Assess the morphology of the erythrocytes.
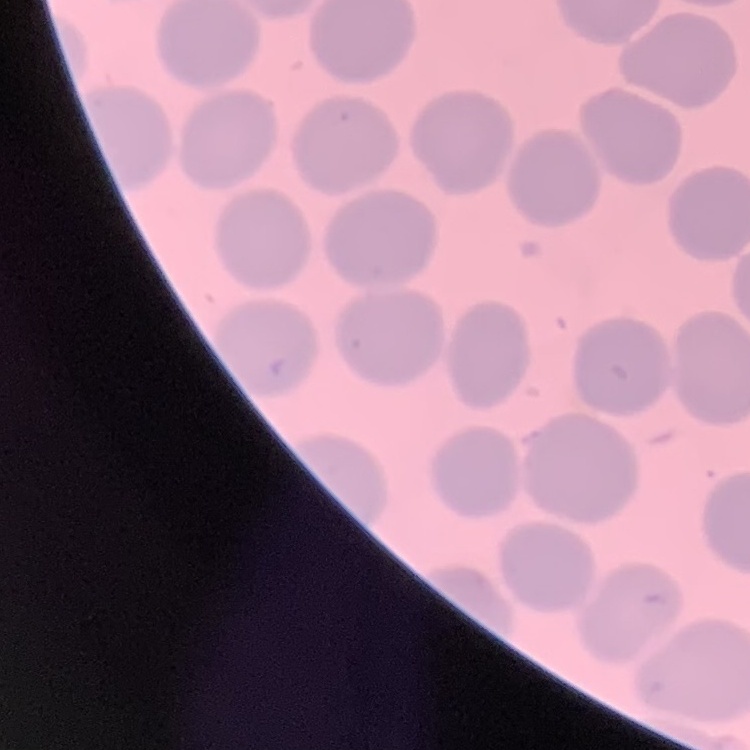

They show no rouleaux formation.

Summary:
  - Stain: Field's or Giemsa
  - Preparation: thin peripheral smear
  - Image type: square crop of a larger photomicrograph